State the preparation type.
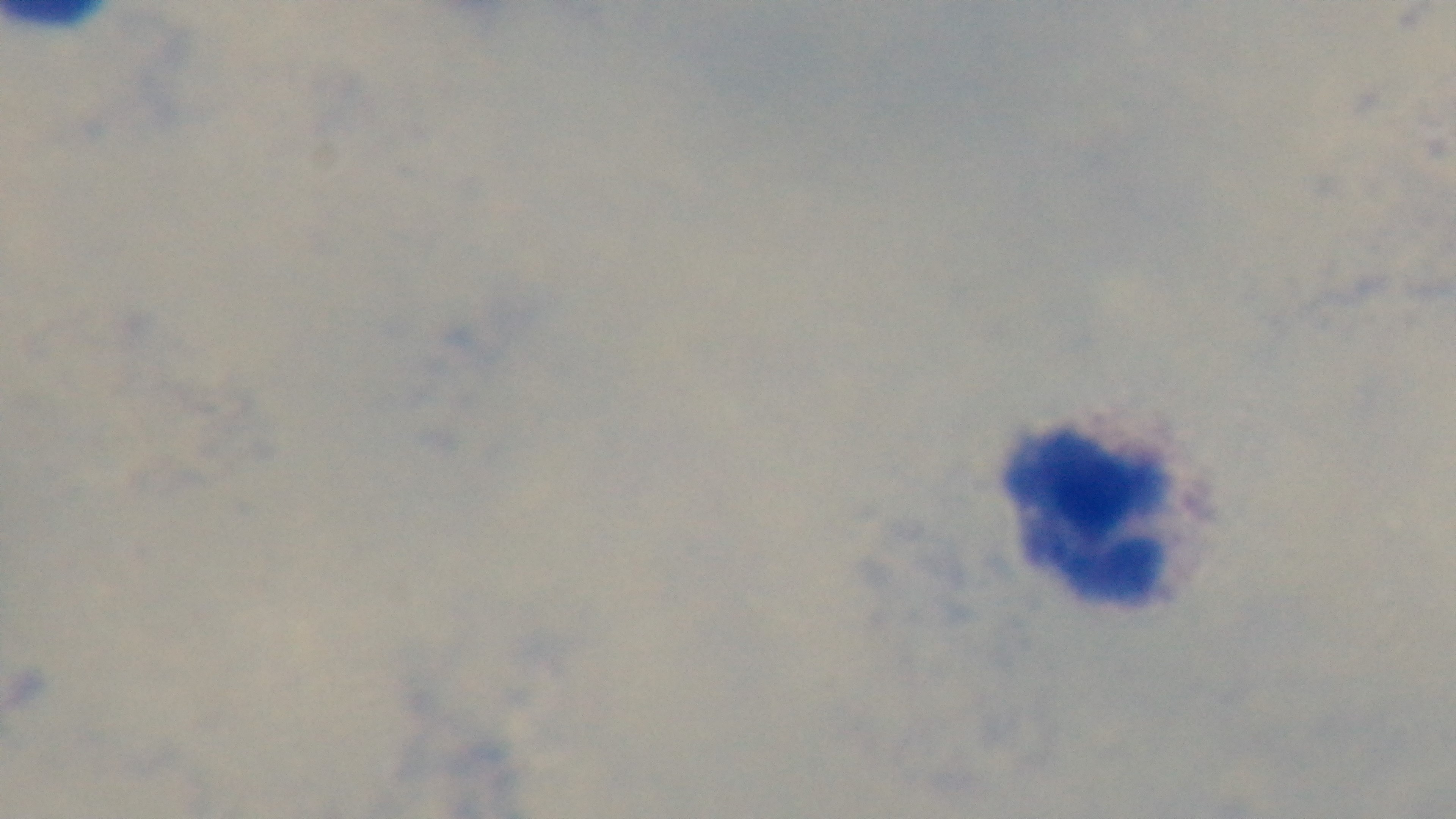
Thick.

Summary:
  - Malaria status: negative
  - Stain: Giemsa
  - Field of view: single
  - Modality: light microscopy
  - Objective: 100x oil immersion
  - Capture: mounted 4K digital camera